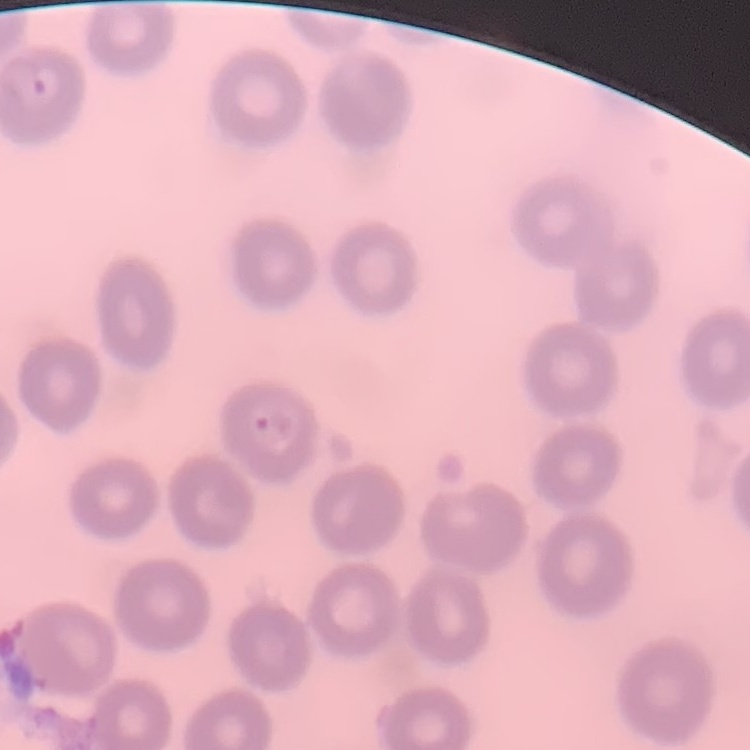

Summary:
  - Red blood cell morphology: no rouleaux formation
  - Image type: one tile cut from a larger photomicrograph
  - Stain: Field's or Giemsa
  - Preparation: thin blood smear